Describe the morphology of the erythrocytes.
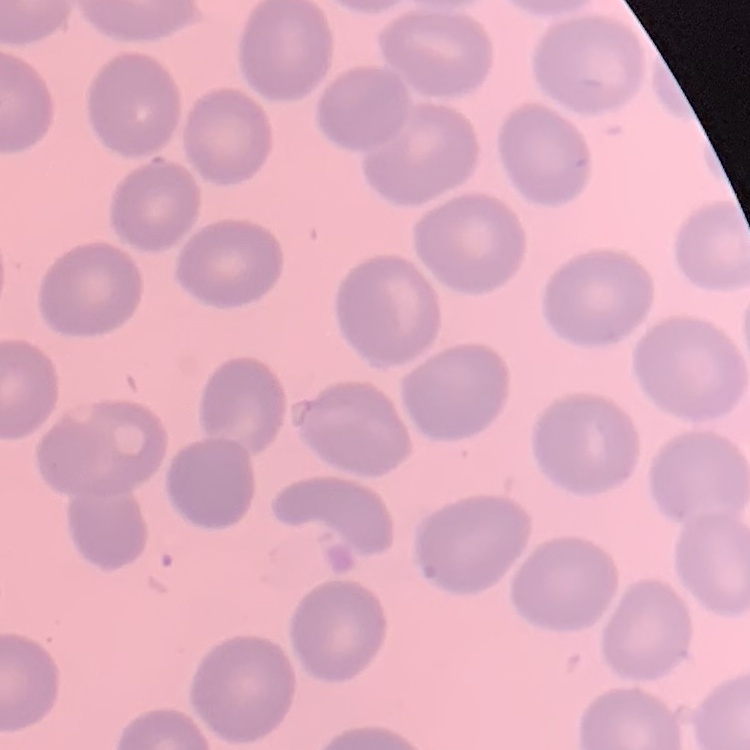

No rouleaux formation.

{
  "preparation": "thin blood film",
  "image_type": "square crop of a larger photomicrograph",
  "stain": "Field's or Giemsa"
}